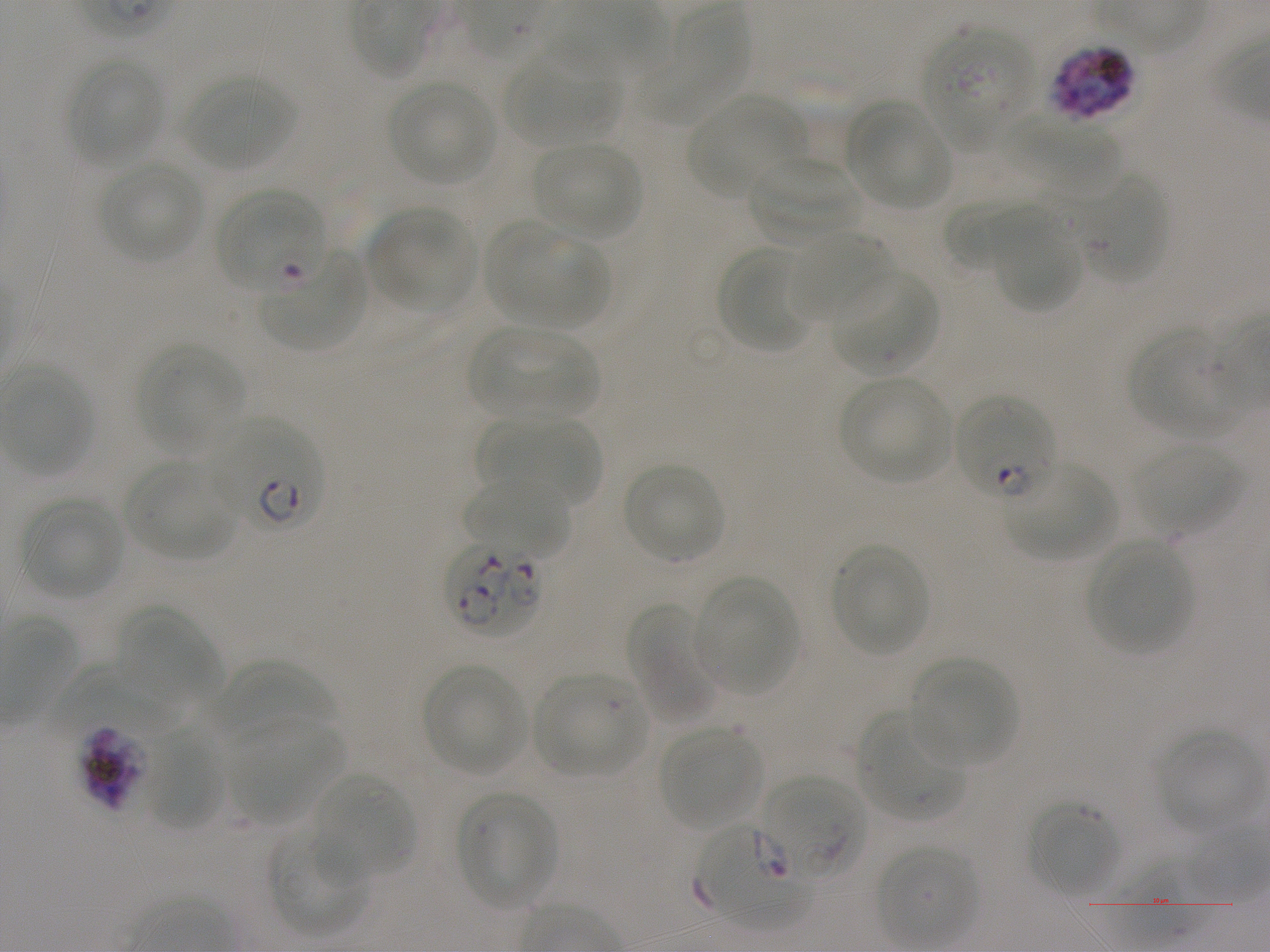
Approximate bounding boxes as [x1, y1, x2, y2] in pixels. Not every red blood cell is marked. A life-cycle stage — or a range of stages, where the recorded stages span more than one — follows each staged infected red blood cell.
Summary:
  - Locations of red blood cells of indeterminate infection status: [922, 26, 1034, 149], [1072, 172, 1165, 283], [215, 178, 327, 284]
  - Locations of uninfected red blood cells: [640, 5, 745, 126], [504, 49, 621, 146], [66, 55, 163, 167], [182, 72, 295, 172], [387, 81, 498, 186], [687, 95, 806, 198], [846, 100, 952, 209], [1001, 113, 1120, 194], [532, 141, 641, 240], [746, 155, 864, 249], [99, 161, 202, 263], [943, 198, 1032, 272], [983, 205, 1084, 311], [367, 208, 473, 312], [485, 224, 608, 329], [789, 229, 893, 320], [716, 244, 815, 355], [830, 270, 940, 376], [466, 326, 599, 421], [1131, 328, 1243, 436], [137, 343, 245, 455], [839, 375, 952, 484], [478, 416, 602, 507], [1132, 443, 1243, 537], [123, 461, 237, 560], [1003, 462, 1117, 560], [622, 463, 726, 563], [463, 476, 571, 558], [19, 497, 125, 599], [1087, 538, 1193, 655], [829, 543, 930, 657], [695, 580, 797, 695], [629, 603, 718, 725], [118, 605, 220, 704], [910, 658, 1016, 768], [213, 662, 336, 745], [422, 663, 526, 774], [47, 665, 190, 738], [532, 673, 648, 777], [855, 710, 962, 823], [226, 719, 342, 823], [658, 726, 764, 831], [1155, 728, 1262, 833], [143, 729, 224, 831], [312, 772, 414, 880], [455, 790, 557, 910], [1029, 802, 1120, 896], [267, 826, 367, 937]
  - Locations of infected red blood cells: [1049, 44, 1137, 121] schizont; [261, 249, 367, 349] early ring; [954, 397, 1055, 503]; [214, 418, 324, 533] ring; [446, 541, 542, 638]; [75, 725, 150, 813] schizont; [762, 776, 866, 884] ring; [695, 825, 812, 928] ring
  - Life-cycle stages observed: ring, schizont
  - Objective: 100x, oil immersion, numerical aperture 1.25
  - Image size: 1270×952 pixels
  - Field of view: single
  - Culture: static in-vitro P. falciparum strain NF54
  - Stain: Giemsa
  - Donor blood group: A+
  - Preparation: thin blood smear